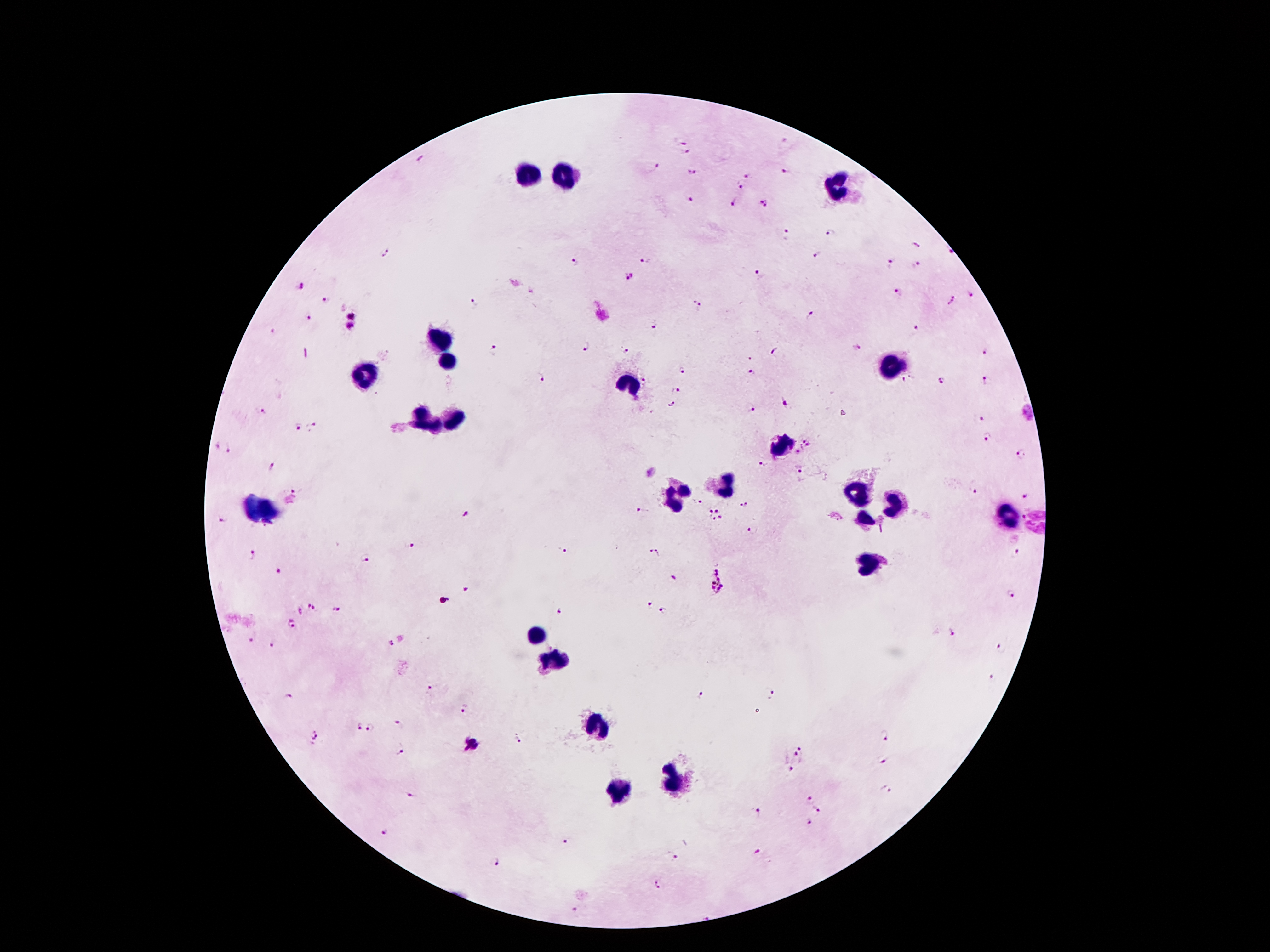

Approximate centers as (x, y) in pixels.
Summary:
  - Leukocyte locations: (525, 171), (563, 171), (836, 187), (441, 343), (448, 358), (891, 364), (362, 377), (631, 384), (452, 416), (421, 421), (780, 446), (717, 484), (855, 494), (676, 495), (898, 503), (1006, 515), (864, 519), (868, 564), (536, 636), (552, 660), (600, 726), (674, 783), (619, 792)
  - Malaria parasite locations: (682, 139), (688, 152), (421, 160), (657, 165), (787, 170), (692, 173), (750, 176), (741, 186), (690, 200), (734, 202), (764, 203), (831, 232), (787, 236), (916, 245), (386, 252), (818, 257), (646, 259), (575, 262), (891, 265), (919, 265), (761, 274), (629, 277), (300, 287), (900, 294), (971, 295), (327, 301), (950, 301), (475, 303), (698, 307), (353, 314), (812, 315), (309, 316), (653, 325), (915, 328), (351, 329), (272, 331), (857, 345), (586, 346), (495, 350), (625, 350), (776, 352), (986, 352), (683, 369), (752, 373), (540, 378), (646, 380), (906, 381), (942, 381), (986, 381), (675, 390), (784, 402), (671, 403), (750, 409), (260, 412), (1026, 412), (980, 418), (299, 426), (315, 426), (988, 437), (806, 449), (230, 451), (1021, 454), (271, 465), (763, 465), (799, 469), (296, 490), (972, 491), (1026, 496), (700, 503), (745, 505), (643, 510), (717, 510), (708, 512), (466, 515), (721, 518), (1023, 518), (223, 520), (713, 520), (753, 531), (412, 546), (565, 550), (651, 550), (660, 552), (252, 554), (1013, 554), (364, 558), (278, 572), (674, 578), (716, 581), (466, 588), (1011, 593), (649, 606), (312, 607), (299, 609), (665, 609), (336, 610), (560, 611), (291, 624), (951, 632), (250, 639), (391, 645), (272, 646), (1001, 649), (992, 680), (429, 687), (769, 692), (701, 694), (287, 699), (465, 708), (401, 725), (356, 727), (371, 729), (317, 735), (883, 735), (519, 738), (799, 749), (400, 750), (883, 758), (790, 769), (410, 793), (810, 800), (818, 809), (759, 812), (809, 821), (384, 831), (563, 840), (756, 852), (676, 857), (497, 861), (656, 885), (576, 912)
  - Magnification: 100x
  - Stain: Giemsa
  - Patient malaria status: positive for Plasmodium falciparum
  - Image size: 1270×952 pixels
  - Preparation: thick peripheral-blood smear
  - Capture: smartphone camera through the microscope eyepiece
  - Field of view: single